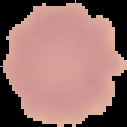

{
  "image_size": "127×127 pixels",
  "image_type": "segmented cell region on a black background",
  "malaria_status": "uninfected",
  "preparation": "thin blood smear"
}